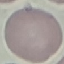

result = negative for malaria parasites
preparation = thin blood film
image type = automatically extracted cell patch, resized to 64 × 64 pixels
stain = Giemsa
capture = smartphone camera at the microscope eyepiece